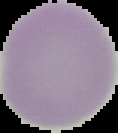
Summary:
  - Image type: segmented cell region on a black background
  - Image size: 118×133 pixels
  - Preparation: thin blood film
  - Result: negative for Plasmodium parasites